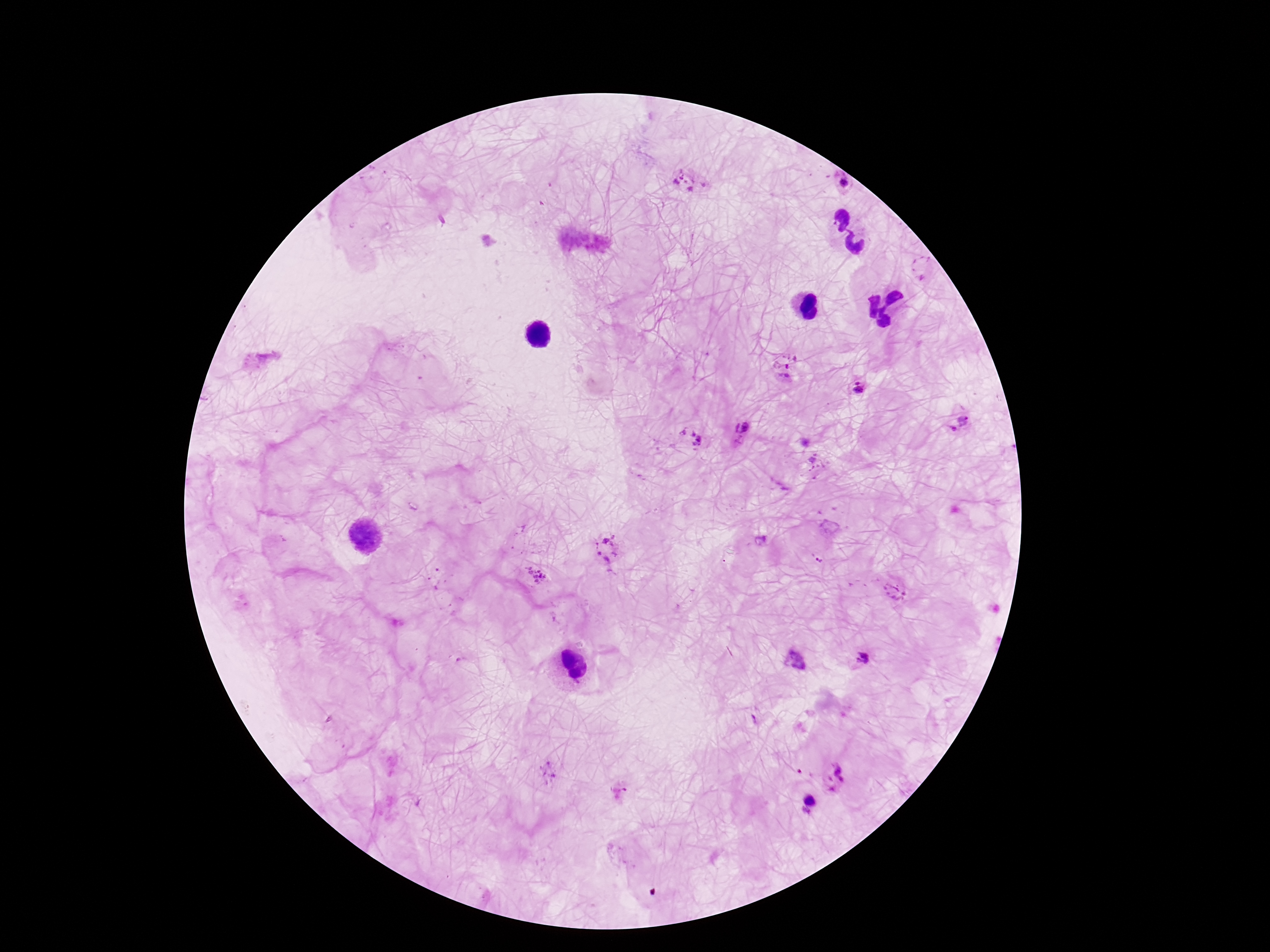
Approximate centers as (x, y) in pixels.
Summary:
  - Plasmodium parasite locations: (685, 182), (839, 184), (782, 369), (855, 387), (963, 424), (742, 433), (688, 441), (605, 549), (537, 575), (895, 594), (860, 658), (834, 777), (803, 806)
  - Stain: Giemsa
  - Image size: 1270×952 pixels
  - Field of view: single
  - Capture: smartphone camera through the microscope eyepiece
  - Patient malaria status: infected
  - Preparation: thick peripheral-blood smear
  - Magnification: 100x